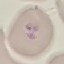 Malaria status: parasitized. Thin smear of blood. Acquired by smartphone through the microscope eyepiece. Automatically extracted cell patch, resized to 64 × 64 pixels. Giemsa stain.